Assess this cell for malaria.
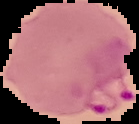

It is parasitized.

From a thin blood film. Image is 139×124 pixels. The area outside the segmented cell region is set to black.